Point out each Plasmodium parasite.
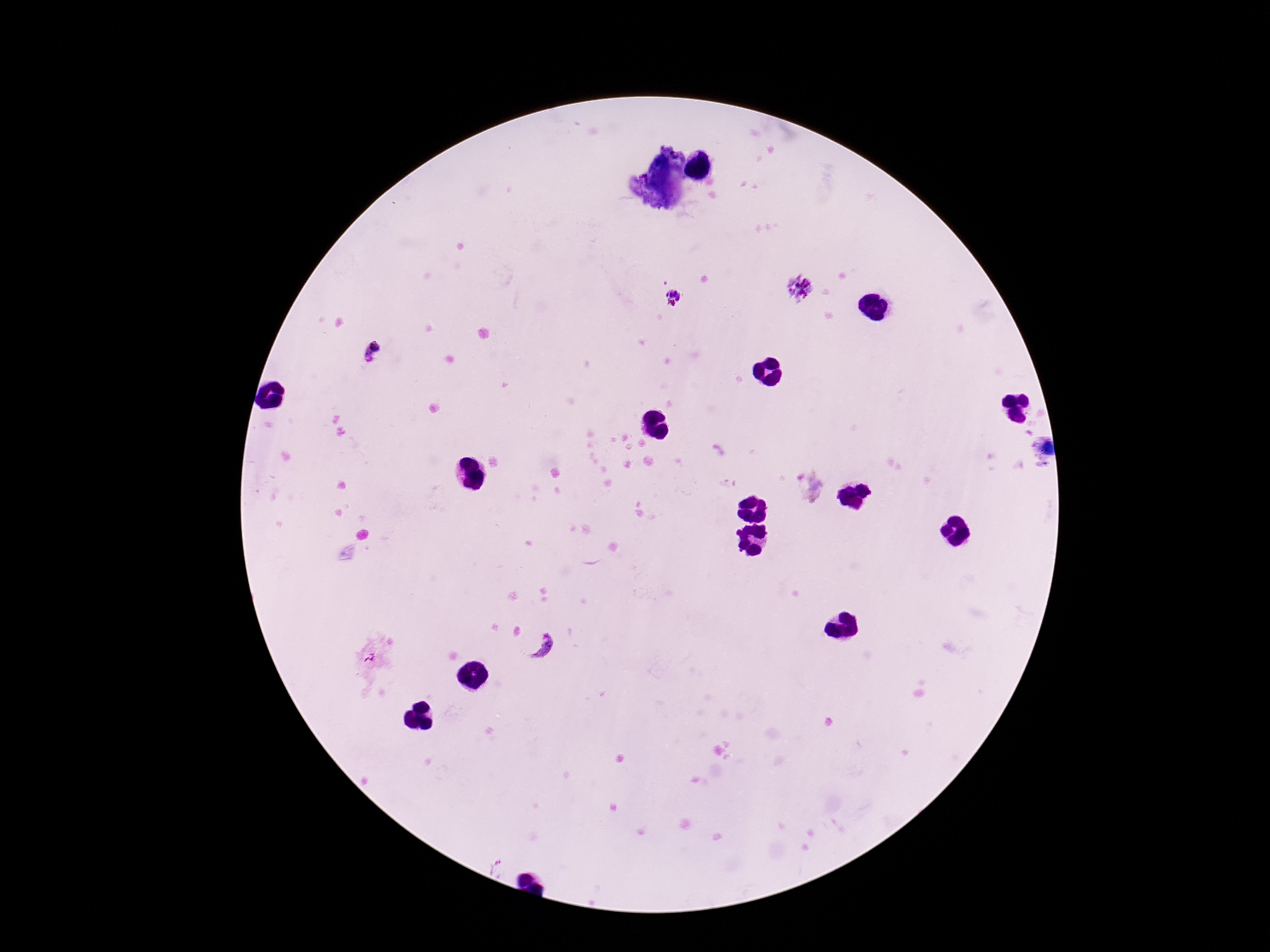

Approximate centers as (x, y) in pixels.
Plasmodium parasites: (799, 286), (673, 298), (374, 353), (809, 486), (541, 645).

field of view = one from this slide
magnification = 100x
patient malaria status = positive
stain = Giemsa
preparation = thick peripheral-blood smear
capture = smartphone camera through the microscope eyepiece
image size = 1270×952 pixels